Locate every malaria parasite and every leukocyte.
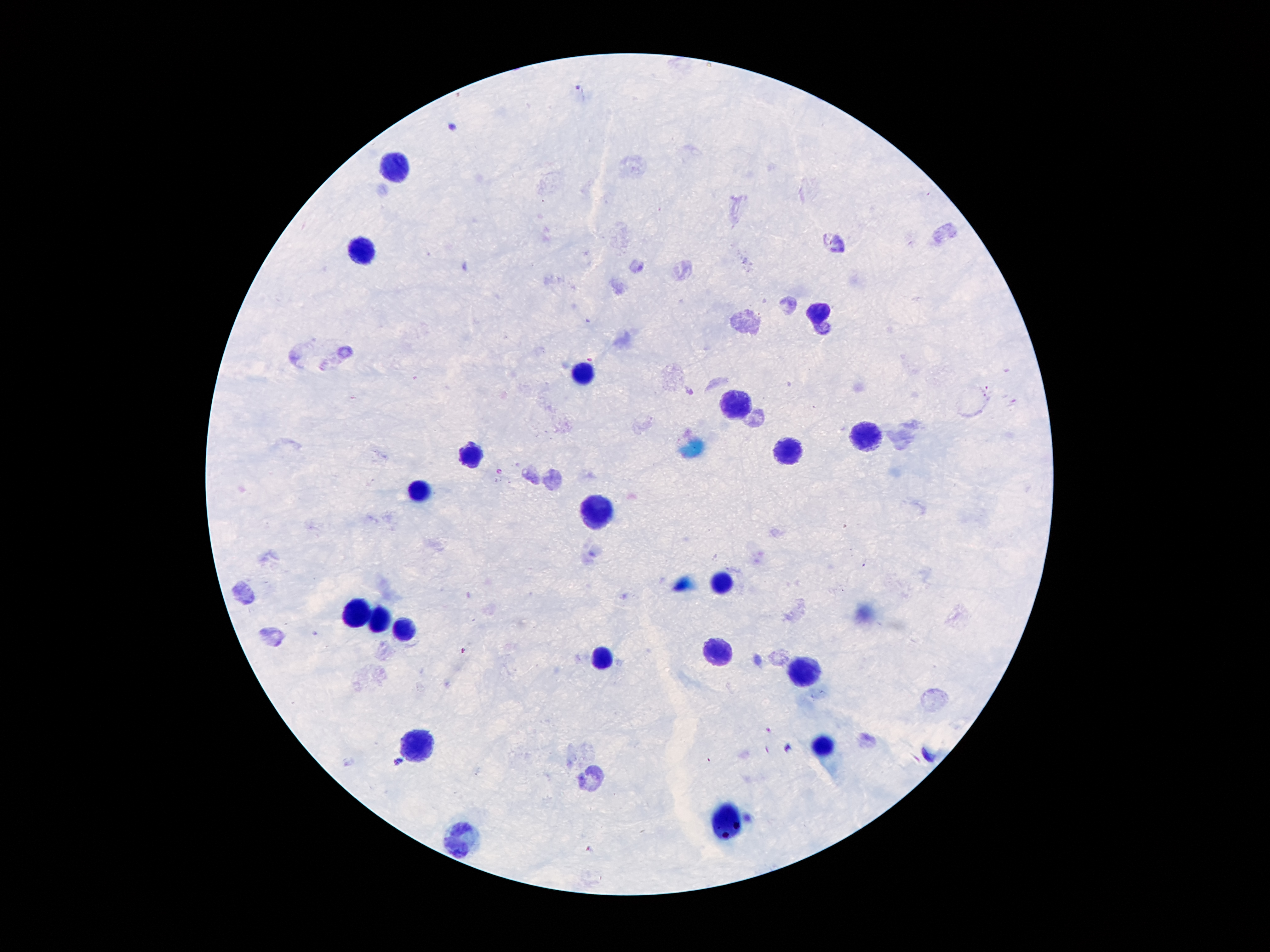

Approximate centers as {x, y} in pixels.
Malaria parasites: {451, 127}, {399, 762}.
Leukocytes: {392, 169}, {364, 253}, {820, 311}, {581, 374}, {730, 405}, {866, 437}, {787, 454}, {467, 456}, {425, 492}, {595, 514}, {719, 583}, {360, 616}, {377, 620}, {402, 629}, {717, 652}, {604, 659}, {805, 668}, {421, 745}, {824, 745}, {726, 823}, {457, 838}.

Summary:
  - Stain: Giemsa
  - Patient malaria status: infected with Plasmodium falciparum
  - Image size: 1270×952 pixels
  - Capture: smartphone through the microscope eyepiece
  - Magnification: 100x
  - Field of view: one from this slide
  - Preparation: thick blood smear